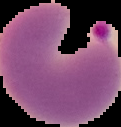
From a thin blood film. Malaria status: parasitized. The area outside the segmented cell region is set to black. Image is 121×127 pixels.